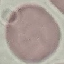

Summary:
  - Result: no malaria parasites seen
  - Preparation: thin smear
  - Image type: cell patch, automatically extracted from a larger field of view and resized to 64 × 64 pixels
  - Capture: smartphone through the microscope eyepiece
  - Stain: Giemsa